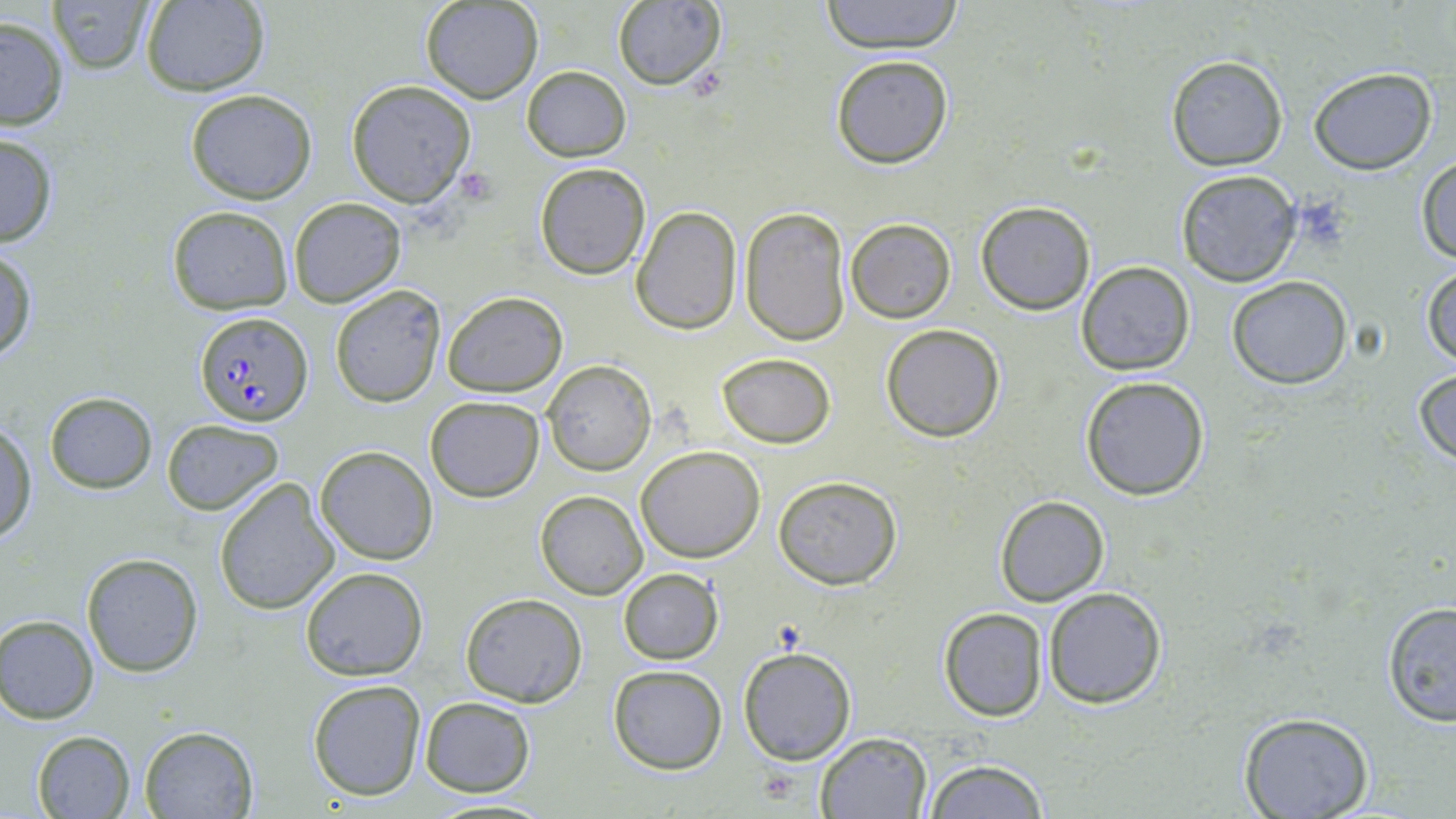
Summary:
  - Coordinate format: approximate bounding boxes as (x1, y1, x2, y2) in pixels
  - Plasmodium falciparum-infected red blood cell locations: (192, 310, 313, 428)
  - Uninfected red blood cell locations: (49, 0, 155, 76), (420, 0, 543, 103), (819, 0, 966, 53), (137, 1, 270, 96), (612, 1, 725, 89), (0, 15, 70, 130), (830, 54, 955, 169), (1164, 55, 1288, 171), (522, 66, 630, 161), (1308, 68, 1437, 174), (345, 80, 478, 206), (185, 91, 317, 205), (0, 132, 60, 249), (1414, 153, 1456, 266), (534, 164, 650, 279), (1174, 170, 1301, 285), (289, 197, 406, 307), (976, 201, 1095, 315), (166, 206, 293, 313), (631, 206, 743, 335), (740, 209, 851, 346), (845, 218, 956, 322), (0, 248, 38, 367), (1077, 261, 1195, 374), (1422, 264, 1455, 371), (1226, 277, 1353, 389), (330, 284, 449, 408), (442, 289, 568, 397), (880, 324, 1006, 443), (715, 352, 836, 447), (542, 360, 656, 476), (1413, 367, 1456, 465), (1081, 375, 1210, 500), (45, 392, 156, 493), (425, 396, 545, 501), (162, 419, 284, 515), (1, 420, 36, 545), (315, 445, 438, 565), (636, 446, 765, 564), (773, 474, 903, 590), (214, 478, 341, 614), (536, 491, 647, 599), (992, 496, 1109, 606), (81, 552, 203, 677), (299, 566, 428, 681), (617, 568, 724, 664), (1042, 587, 1167, 709), (460, 592, 587, 707), (1379, 599, 1456, 729), (937, 607, 1049, 722), (0, 614, 100, 723), (737, 645, 857, 766), (607, 665, 727, 774), (307, 678, 426, 801), (418, 695, 537, 798), (1237, 712, 1375, 819), (138, 725, 258, 818), (31, 731, 136, 819), (816, 732, 931, 819), (924, 758, 1052, 819)
  - Platelet locations: (457, 168, 498, 203)
  - Slide-level diagnosis: Plasmodium falciparum
  - Field of view: single
  - Preparation: thin blood film
  - Modality: light microscopy
  - Stain: May-Grünwald-Giemsa
  - Magnification: 1000x
  - Image size: 1456×819 pixels